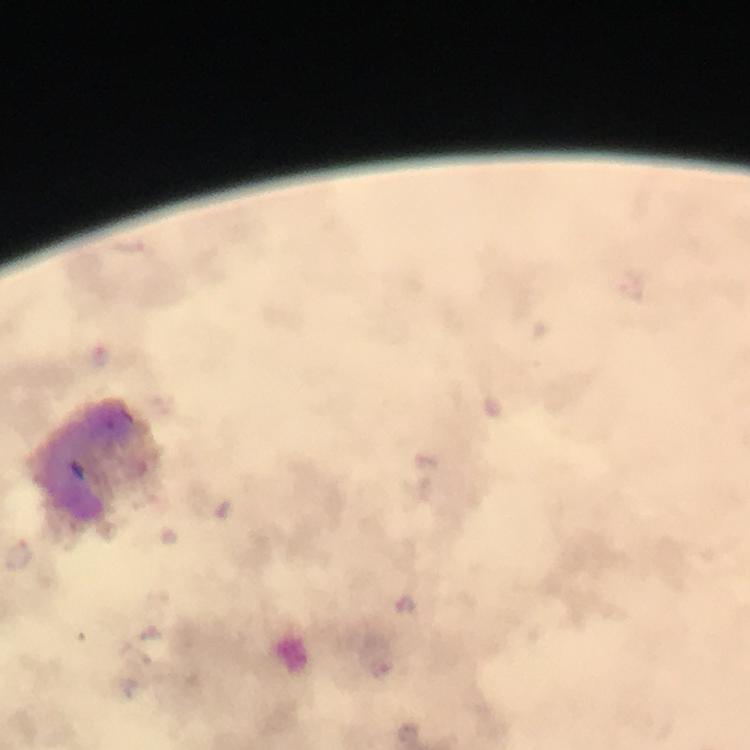

stain: Giemsa
cropped_from: one field of view
plasmodium_parasite_locations: 'approximate object centers, in pixels from the top-left corner: (x=100, y=358), (x=406, y=605)'
context: from a malaria diagnostic workup
magnification: 100x
capture: smartphone camera through the microscope
image_size: 750×750 pixels
immersion_oil: used
leukocyte_locations: 'approximate object centers, in pixels from the top-left corner: (x=84, y=462)'
preparation: thick smear